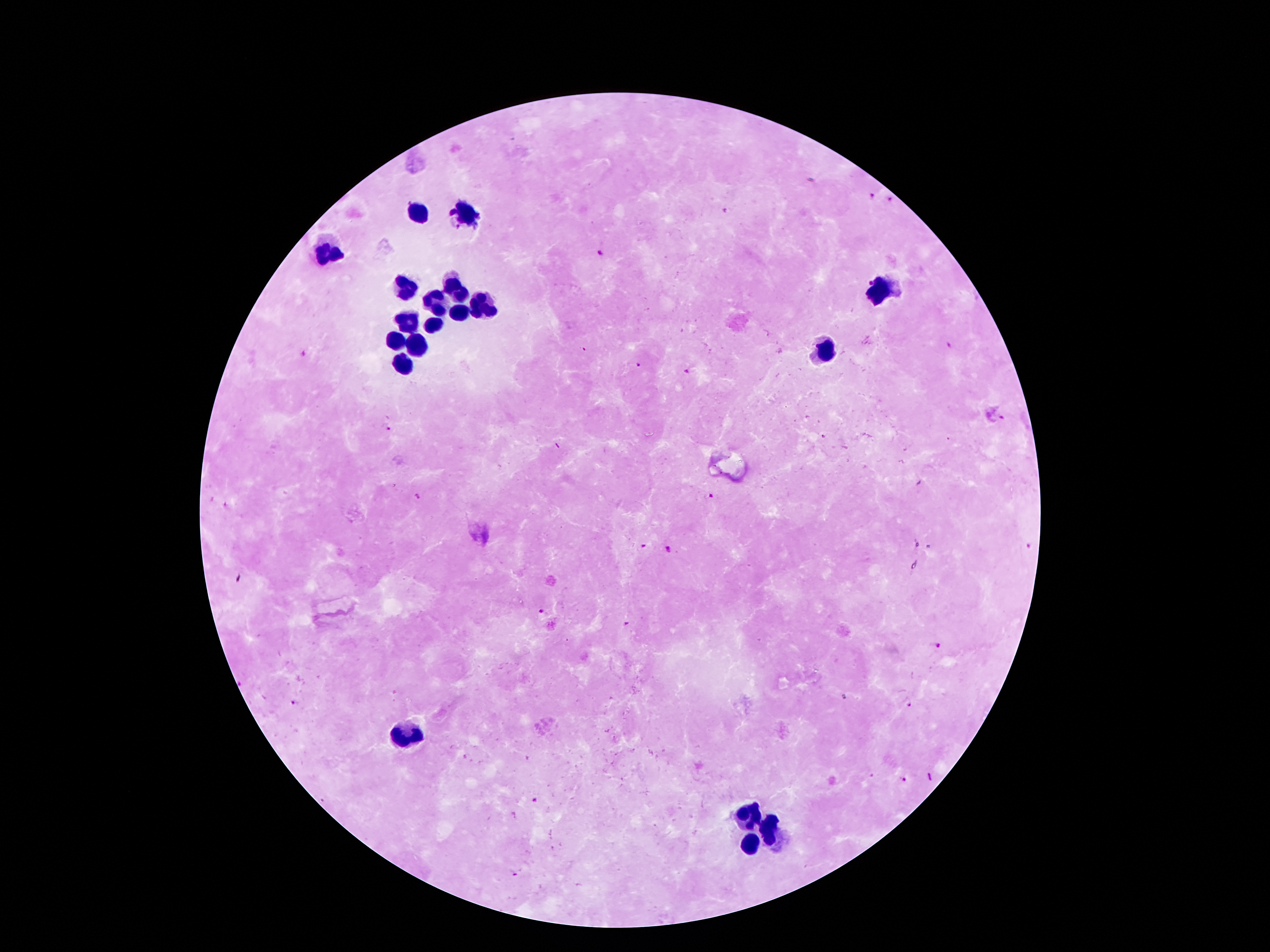
Approximate centers as (x, y) in pixels.
Summary:
  - Leukocyte locations: (463, 212), (418, 214), (323, 251), (407, 283), (459, 290), (879, 293), (484, 303), (438, 304), (456, 311), (409, 321), (432, 324), (394, 339), (416, 342), (823, 353), (403, 365), (410, 737), (746, 812), (769, 828), (750, 844)
  - Malaria parasite locations: (872, 197), (889, 202), (722, 211), (598, 253), (950, 346), (302, 355), (639, 365), (686, 371), (1002, 418), (387, 430), (919, 482), (711, 496), (417, 497), (644, 546), (669, 549), (540, 611), (626, 624), (937, 646), (294, 702), (910, 705), (930, 776), (902, 779), (532, 801)
  - Stain: Giemsa
  - Capture: smartphone camera through the microscope eyepiece
  - Image size: 1270×952 pixels
  - Magnification: 100x
  - Preparation: thick blood film
  - Field of view: single
  - Patient malaria status: infected with Plasmodium falciparum